Report the malaria status of this cell.
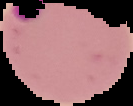
Parasitized.

Segmented cell region on a black background. Image is 133×106 pixels. From a thin blood smear.